Give the extent of all uninfected red blood cells.
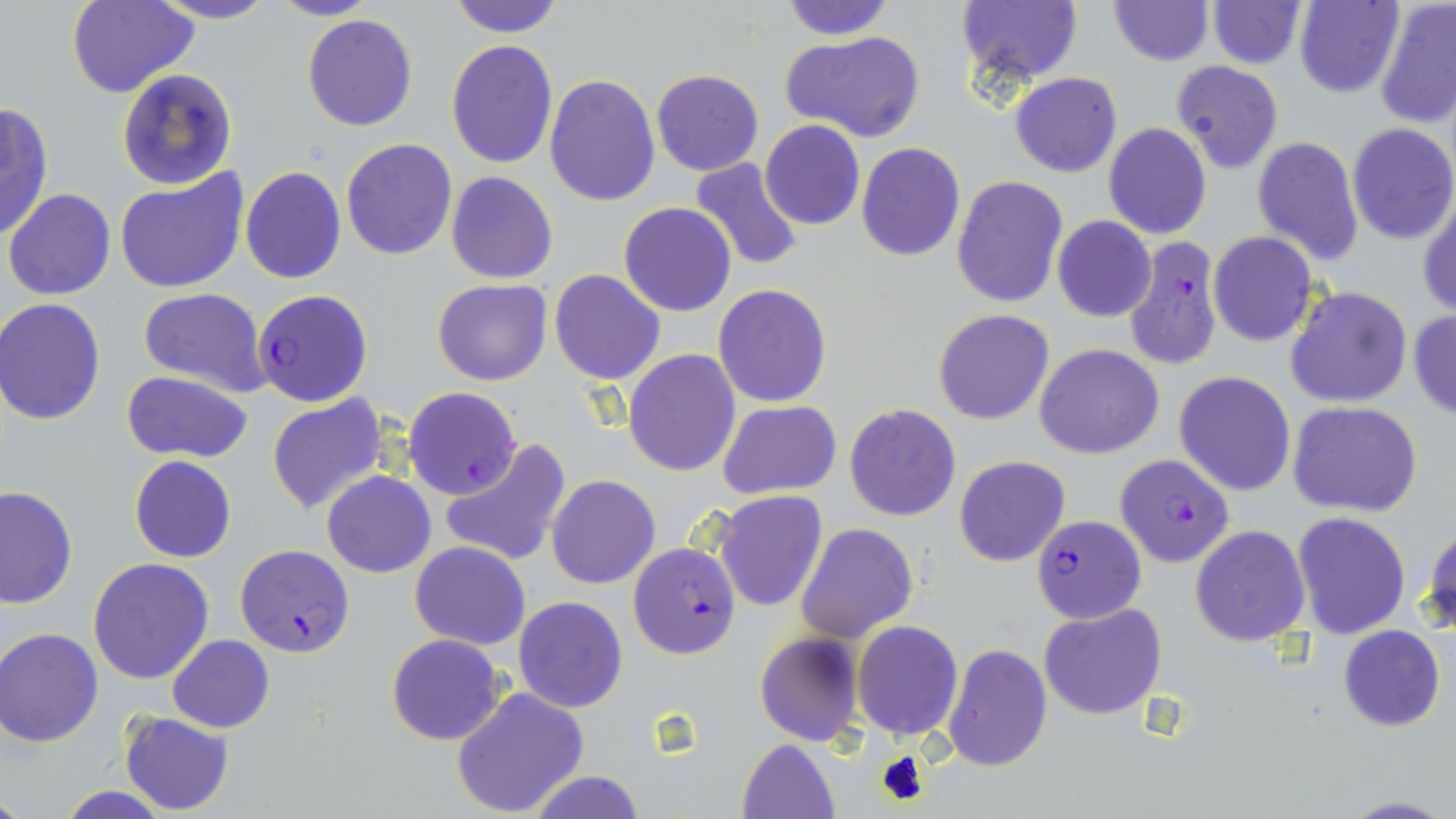

Approximate bounding boxes as (x1, y1, x2, y2) in pixels.
Uninfected red blood cells: (67, 0, 199, 99), (146, 0, 279, 25), (268, 0, 377, 22), (777, 0, 896, 40), (955, 0, 1087, 90), (1107, 0, 1213, 66), (1207, 0, 1307, 69), (1295, 0, 1404, 98), (1375, 0, 1456, 128), (446, 1, 566, 37), (302, 14, 417, 132), (779, 29, 925, 143), (444, 40, 560, 169), (1172, 60, 1284, 174), (116, 67, 239, 192), (651, 68, 763, 176), (1008, 71, 1123, 176), (544, 74, 662, 208), (0, 101, 54, 243), (759, 121, 866, 231), (1102, 122, 1212, 240), (1345, 123, 1456, 245), (1251, 135, 1363, 267), (340, 138, 457, 260), (857, 143, 966, 261), (688, 157, 803, 272), (239, 165, 347, 286), (114, 168, 249, 293), (446, 171, 558, 284), (951, 176, 1068, 307), (4, 189, 117, 300), (1418, 195, 1456, 317), (618, 203, 737, 318), (1052, 215, 1157, 322), (1206, 230, 1318, 347), (549, 269, 666, 386), (431, 279, 552, 386), (1284, 284, 1413, 409), (712, 285, 832, 408), (137, 287, 269, 396), (1, 299, 106, 425), (932, 308, 1055, 425), (1407, 308, 1456, 418), (1034, 343, 1165, 459), (624, 350, 741, 477), (1173, 370, 1295, 497), (121, 372, 256, 464), (265, 395, 390, 519), (717, 400, 841, 499), (1288, 401, 1424, 517), (844, 403, 962, 521), (440, 439, 572, 568), (954, 455, 1070, 567), (129, 456, 236, 563), (321, 470, 436, 577), (547, 475, 661, 589), (0, 485, 77, 609), (713, 490, 828, 613), (1292, 512, 1410, 639), (796, 522, 919, 644), (1424, 522, 1456, 638), (1189, 525, 1310, 646), (409, 541, 531, 649), (87, 557, 215, 685), (513, 596, 628, 713), (1038, 603, 1167, 719), (852, 620, 962, 739), (1337, 625, 1445, 732), (0, 628, 104, 746), (753, 631, 864, 747), (384, 633, 508, 746), (167, 635, 274, 733), (941, 643, 1053, 772), (450, 688, 590, 816), (120, 711, 234, 815), (736, 738, 840, 819), (524, 771, 650, 818), (56, 786, 171, 818), (1335, 794, 1453, 817).

Summary:
  - Plasmodium falciparum-infected red blood cell locations: (1123, 237, 1224, 371), (251, 288, 373, 407), (402, 387, 522, 500), (1115, 453, 1235, 567), (1030, 516, 1146, 625), (627, 542, 741, 658), (235, 544, 355, 657)
  - Slide-level diagnosis: Plasmodium falciparum
  - Magnification: 1000x
  - Modality: optical microscopy
  - Field of view: single
  - Preparation: thin blood film
  - Image size: 1456×819 pixels
  - Stain: May-Grünwald-Giemsa